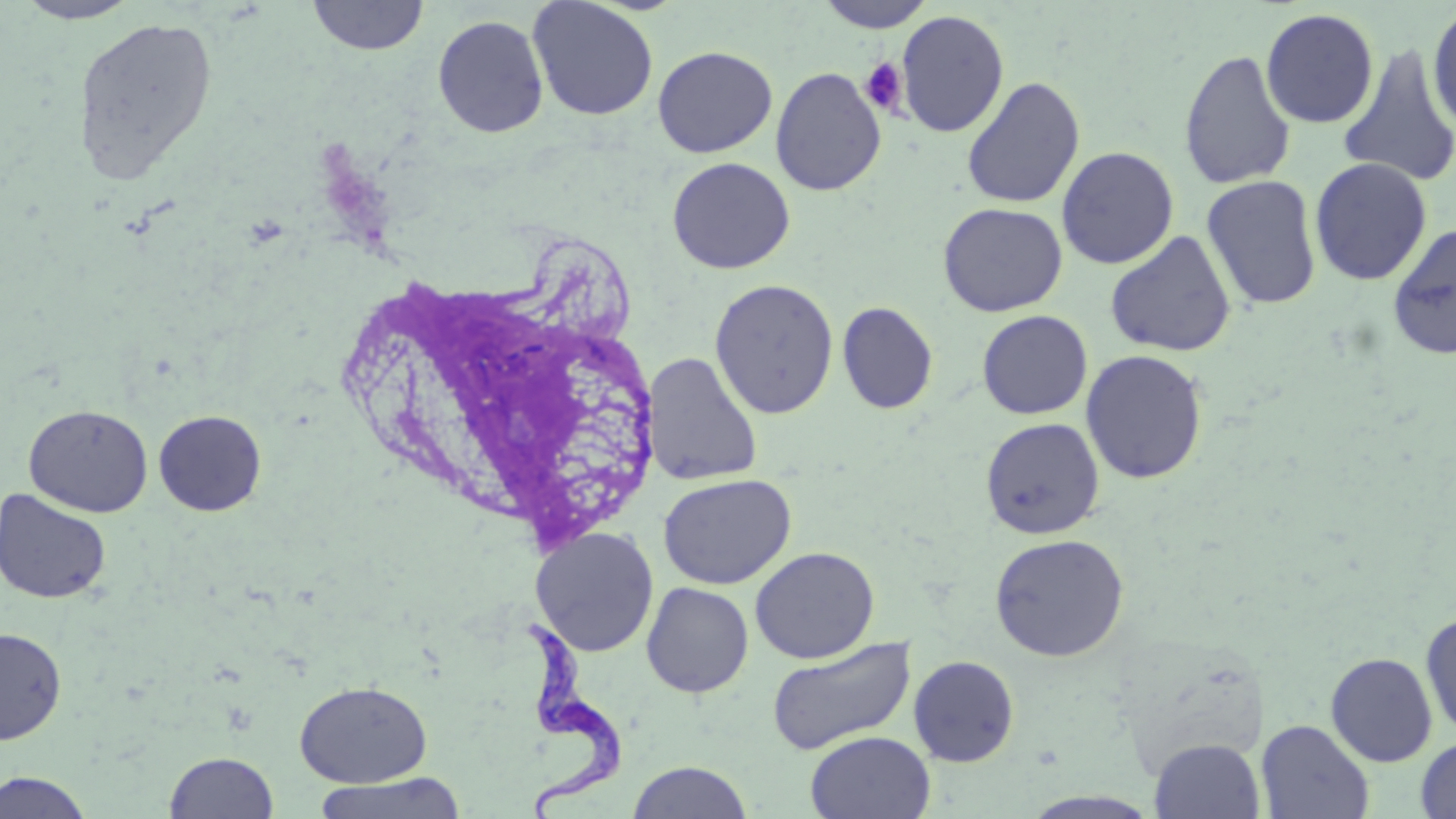
Approximate bounding boxes as named x1/y1/x2/y2 corners in pixels. Trypanosoma brucei locations: (x1=513, y1=616, x2=631, y2=816). Uninfected red blood cell locations: (x1=11, y1=0, x2=143, y2=24), (x1=307, y1=0, x2=430, y2=56), (x1=527, y1=0, x2=659, y2=121), (x1=814, y1=0, x2=936, y2=32), (x1=1426, y1=2, x2=1456, y2=137), (x1=1260, y1=8, x2=1380, y2=129), (x1=895, y1=10, x2=1009, y2=138), (x1=432, y1=14, x2=549, y2=138), (x1=73, y1=15, x2=219, y2=186), (x1=1336, y1=43, x2=1456, y2=189), (x1=652, y1=45, x2=777, y2=158), (x1=1178, y1=48, x2=1297, y2=190), (x1=770, y1=67, x2=887, y2=196), (x1=961, y1=77, x2=1085, y2=208), (x1=1056, y1=146, x2=1179, y2=269), (x1=666, y1=157, x2=795, y2=274), (x1=1309, y1=157, x2=1433, y2=286), (x1=1201, y1=175, x2=1323, y2=310), (x1=938, y1=202, x2=1067, y2=317), (x1=1386, y1=222, x2=1456, y2=361), (x1=1105, y1=230, x2=1236, y2=358), (x1=709, y1=278, x2=839, y2=419), (x1=837, y1=301, x2=938, y2=414), (x1=977, y1=310, x2=1092, y2=419), (x1=1080, y1=349, x2=1208, y2=484), (x1=642, y1=352, x2=763, y2=486), (x1=23, y1=404, x2=153, y2=517), (x1=153, y1=409, x2=267, y2=516), (x1=980, y1=417, x2=1104, y2=539), (x1=658, y1=473, x2=796, y2=589), (x1=0, y1=488, x2=112, y2=604), (x1=531, y1=527, x2=659, y2=657), (x1=990, y1=533, x2=1129, y2=662), (x1=749, y1=546, x2=880, y2=664), (x1=641, y1=582, x2=754, y2=698), (x1=1420, y1=611, x2=1456, y2=739), (x1=0, y1=627, x2=66, y2=744), (x1=766, y1=637, x2=917, y2=756), (x1=1325, y1=652, x2=1437, y2=766), (x1=908, y1=655, x2=1020, y2=766), (x1=294, y1=680, x2=431, y2=787), (x1=1256, y1=719, x2=1374, y2=818), (x1=805, y1=731, x2=936, y2=819), (x1=1416, y1=736, x2=1456, y2=819), (x1=1149, y1=737, x2=1265, y2=819), (x1=164, y1=750, x2=278, y2=818), (x1=627, y1=760, x2=753, y2=819), (x1=0, y1=770, x2=95, y2=818), (x1=312, y1=771, x2=469, y2=819). Platelet locations: (x1=859, y1=56, x2=908, y2=116). Slide-level diagnosis: Trypanosoma brucei. 1000x magnification. Image is 1456×819 pixels. Single field of view. May-Grünwald-Giemsa-stained preparation. Thin blood film. Optical microscopy.